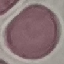
Result: negative for malaria parasites. Photographed with a smartphone camera at the microscope eyepiece. Giemsa-stained preparation. Automatically extracted cell patch, resized to 64 × 64 pixels. Thin smear of blood.